Assess this cell for malaria.
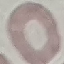

Uninfected.

stain: Giemsa
capture: smartphone camera at the microscope eyepiece
image_type: automatically extracted cell patch, resized to 64 × 64 pixels
preparation: thin blood film